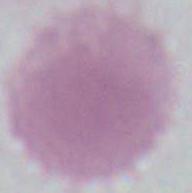 Photomicrograph. A red blood cell is shown. 1000x magnification.